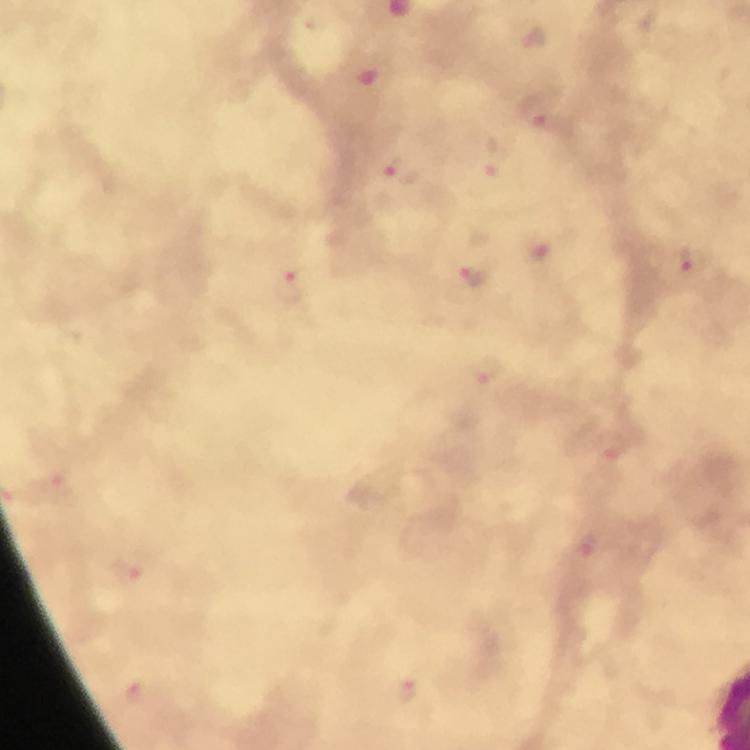
capture = smartphone photograph through a microscope
stain = Giemsa
cropped from = a single field of view
immersion oil = used
context = from a malaria diagnostic workup
magnification = 100x
image size = 750×750 pixels
preparation = thick smear
Plasmodium parasite locations = approximate centers as [x, y] in pixels: [533, 110], [496, 158], [406, 172], [691, 261], [473, 275], [290, 287], [486, 372], [612, 448], [588, 547], [407, 693]